Classify this cell by malaria status.
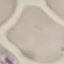
Uninfected.

Summary:
  - Preparation: thin smear
  - Stain: Giemsa
  - Image type: automatically extracted cell patch, resized to 64 × 64 pixels
  - Capture: smartphone camera at the microscope eyepiece